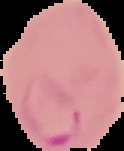 Image is 124×151 pixels. Malaria status: parasitized. From a thin blood film. Segmented cell region on a black background.